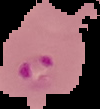

malaria status = parasitized
image size = 100×109 pixels
image type = segmented cell region on a black background
preparation = thin blood film